Identify the parasite.
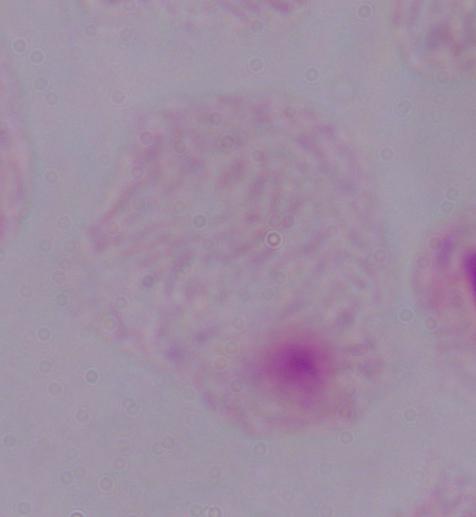

This is a trichomonad.

{
  "magnification": "1000x",
  "modality": "photomicrograph"
}